Describe the morphology of the erythrocytes.
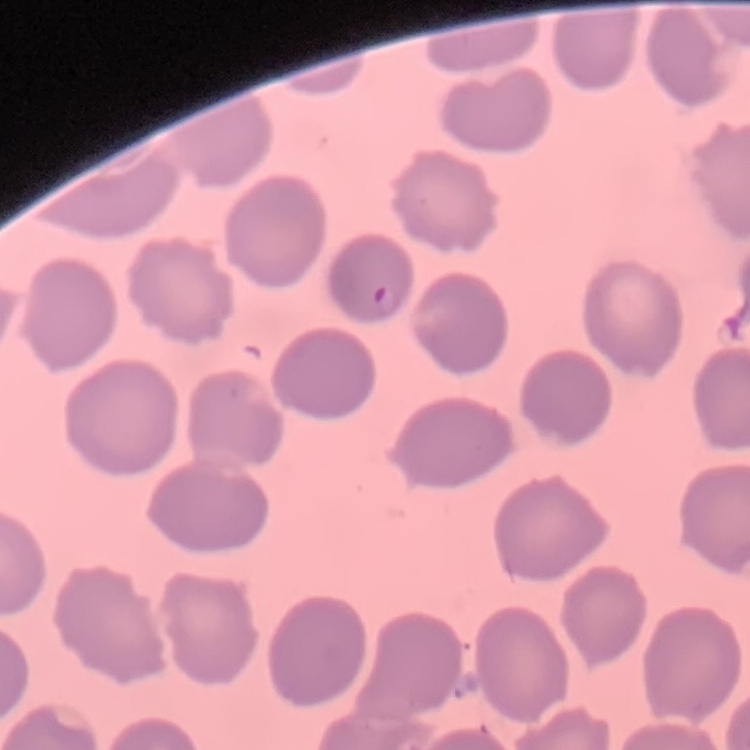
No rouleaux formation.

Summary:
  - Stain: Field's or Giemsa
  - Image type: one tile cut from a larger photomicrograph
  - Preparation: thin peripheral smear